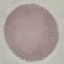 Result: negative for malaria parasites. Giemsa-stained preparation. Thin blood smear. Cell patch, automatically extracted from a larger field of view and resized to 64 × 64 pixels. Photographed with a smartphone camera at the microscope eyepiece.